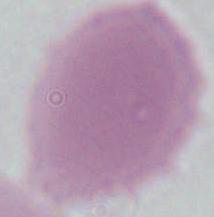

Summary:
  - Modality: micrograph
  - Magnification: 1000x
  - Identification: erythrocyte